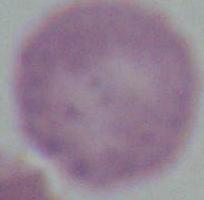

{
  "modality": "photomicrograph",
  "magnification": "1000x",
  "identification": "red blood cell"
}